Report the malaria status of this cell.
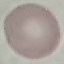

It is uninfected.

Thin blood smear. Cell patch, automatically extracted from a larger field of view and resized to 64 × 64 pixels. Photographed with a smartphone camera at the microscope eyepiece. Giemsa-stained preparation.